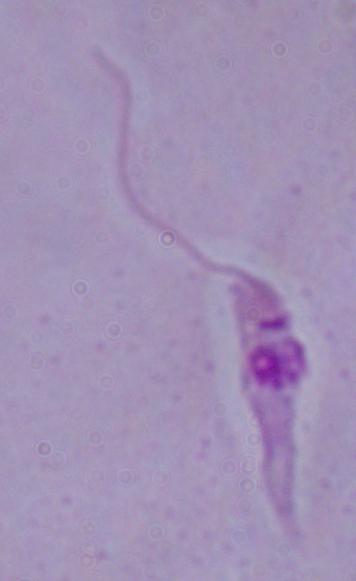

{
  "identification": "Leishmania",
  "magnification": "1000x",
  "modality": "photomicrograph"
}